Assess the morphology of the erythrocytes.
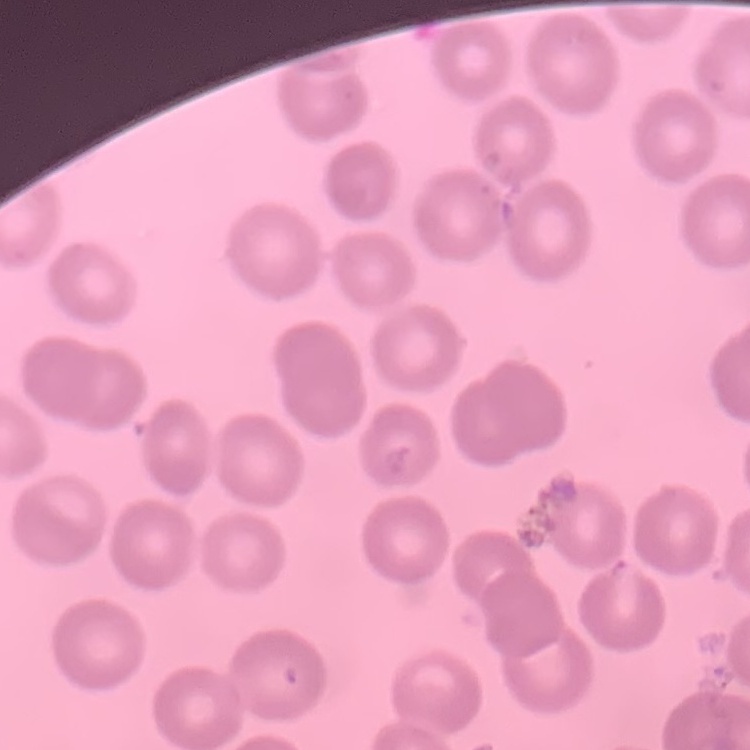

No rouleaux formation.

preparation = thin blood smear
stain = Field's or Giemsa
image type = square crop of a larger photomicrograph